Comment on the morphology of the red blood cells.
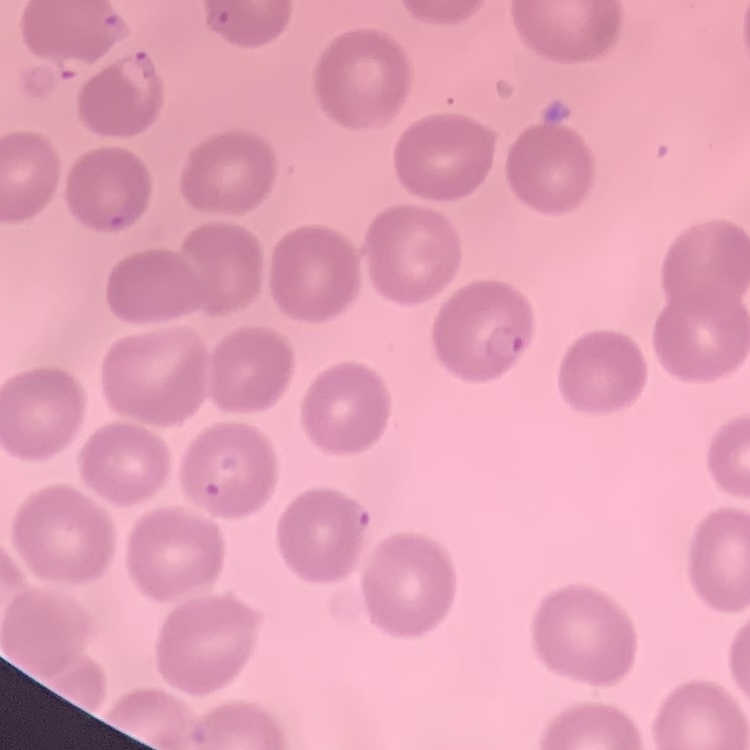

They show no rouleaux formation.

image type = one tile cut from a larger photomicrograph
stain = Field's or Giemsa
preparation = thin blood film